Identify the parasite.
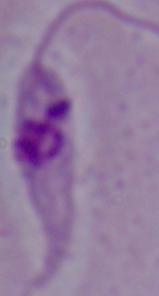
Leishmania.

Summary:
  - Magnification: 1000x
  - Modality: micrograph